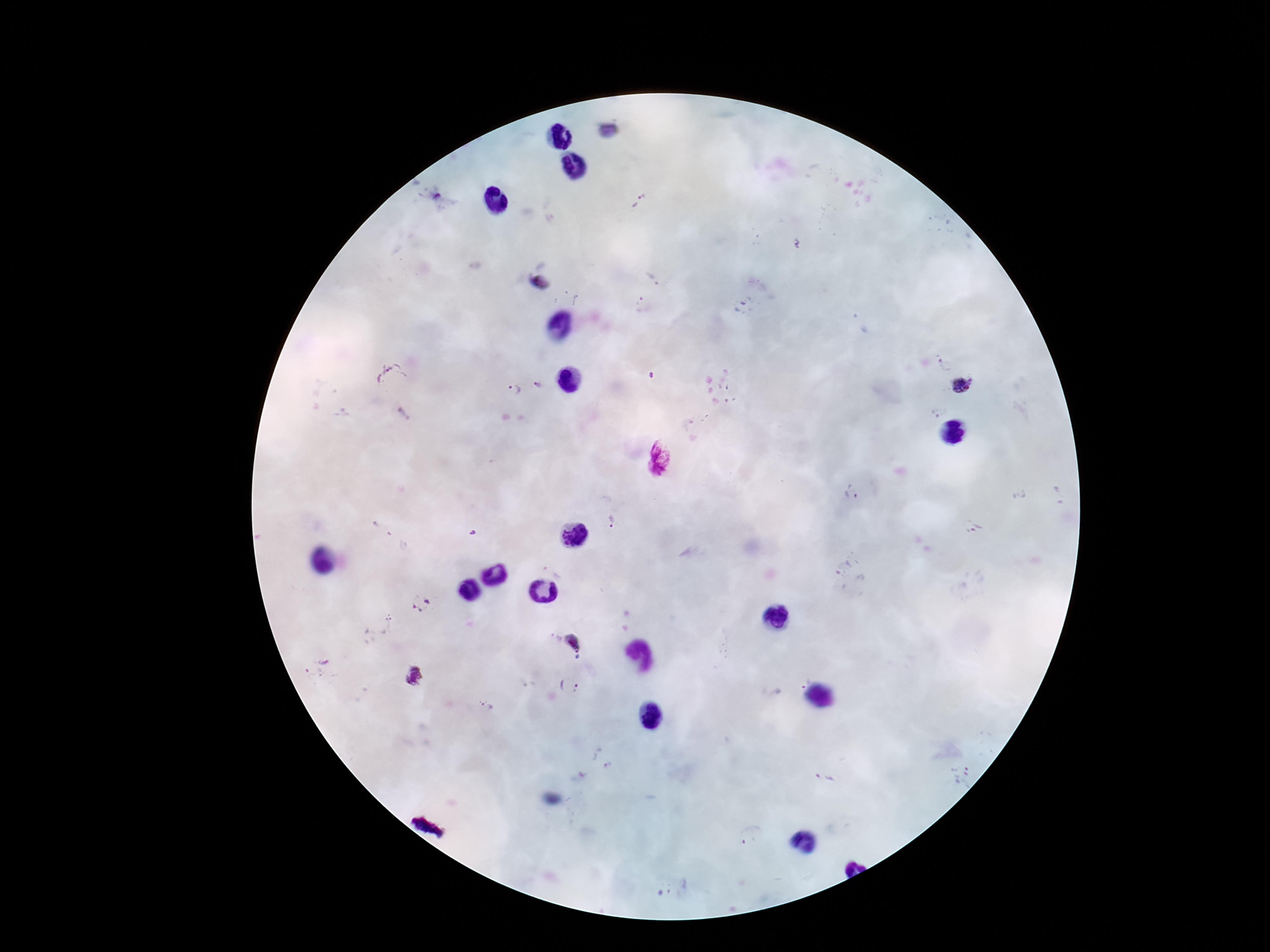

Approximate centers as [x, y] in pixels. Plasmodium parasite locations: [435, 196], [639, 202], [651, 278], [541, 283], [641, 307], [942, 364], [388, 375], [537, 385], [961, 386], [513, 391], [659, 460], [852, 493], [613, 521], [970, 529], [847, 569], [422, 603], [377, 625], [555, 637], [574, 641], [578, 658], [317, 668], [414, 675], [802, 679], [569, 687], [488, 707], [961, 774], [824, 779], [752, 836], [663, 892]. Patient malaria status: infected. Single field of view. Giemsa-stained preparation. Smartphone photograph taken through the microscope eyepiece. Thick blood film. Image is 1270×952 pixels. 100x magnification.